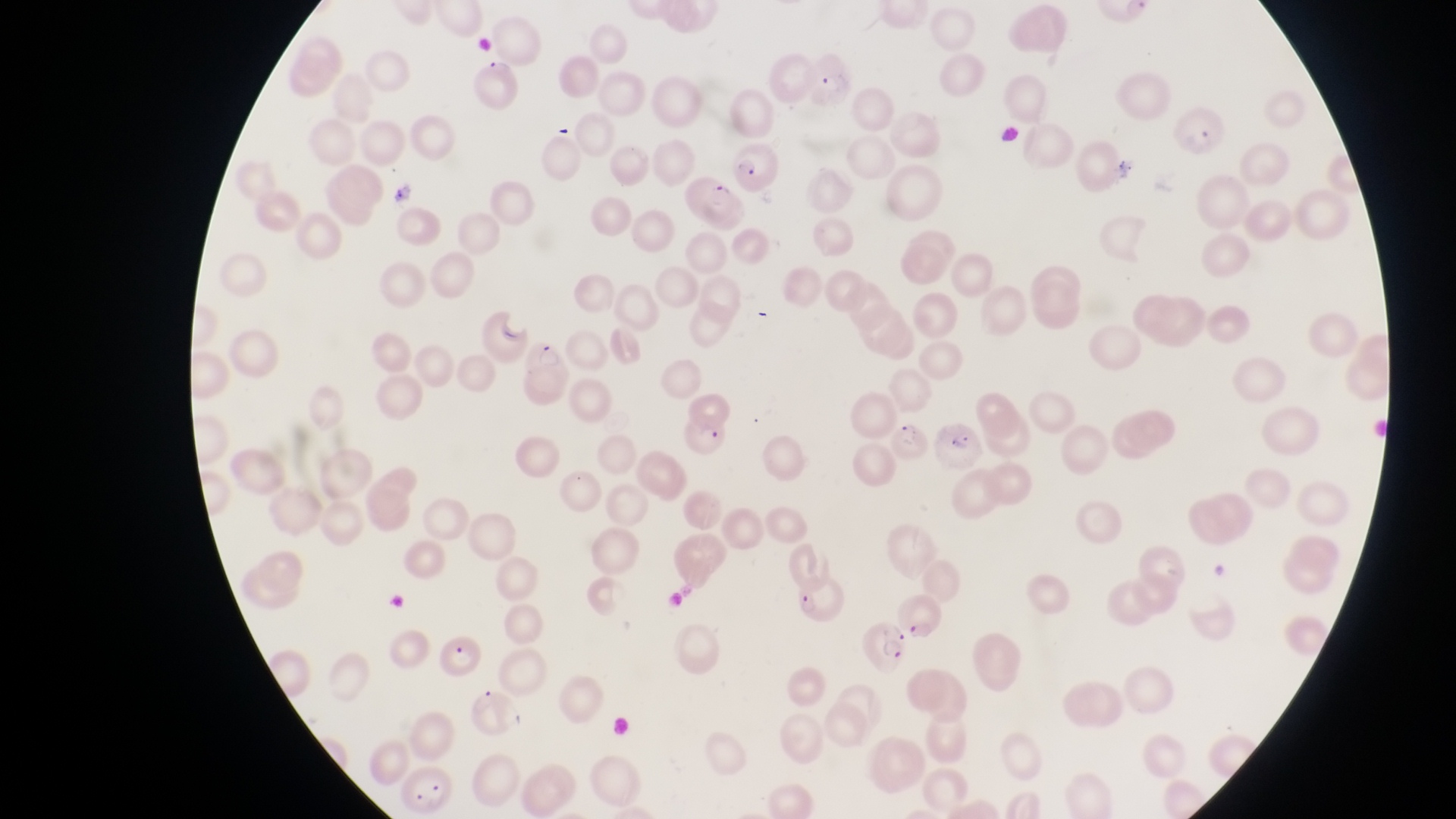 Approximate bounding boxes as {left, top, right, bottom} in pixels. Parasitised red blood cell locations: {682, 175, 741, 231}, {523, 337, 570, 404}, {667, 407, 733, 460}, {935, 420, 988, 475}, {861, 616, 913, 674}, {436, 629, 489, 679}, {399, 761, 453, 813}. Artifact (platelet-like body, stain precipitate, or debris) locations: {389, 178, 418, 202}. Magnification of 1000x. Thin blood smear. Collected in Uganda. Photographed through the eyepiece of an Olympus CX-23 microscope with a smartphone camera. Image is 1456×819 pixels. One field of view.